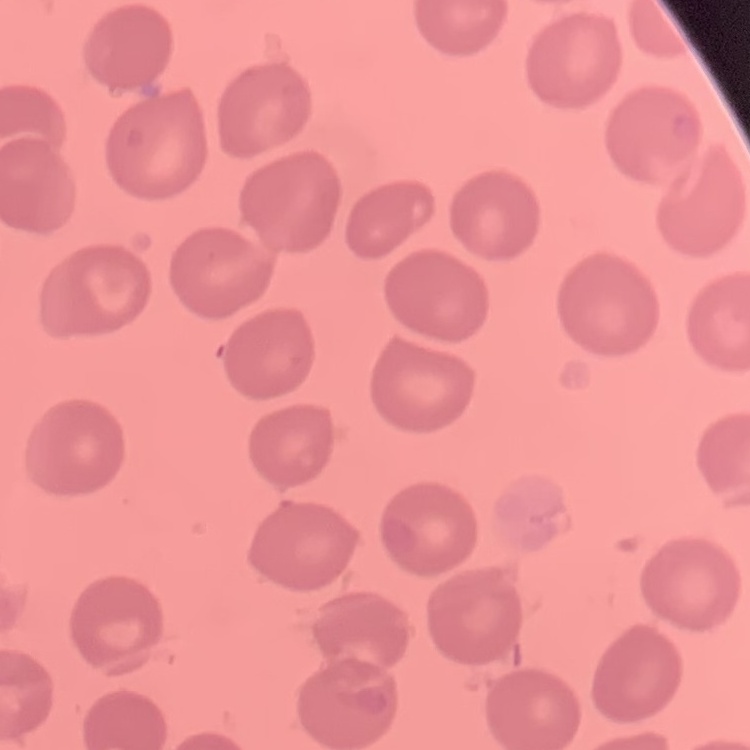

Summary:
  - Erythrocyte morphology: no rouleaux formation
  - Image type: square crop of a larger photomicrograph
  - Stain: Field's or Giemsa
  - Preparation: thin peripheral smear